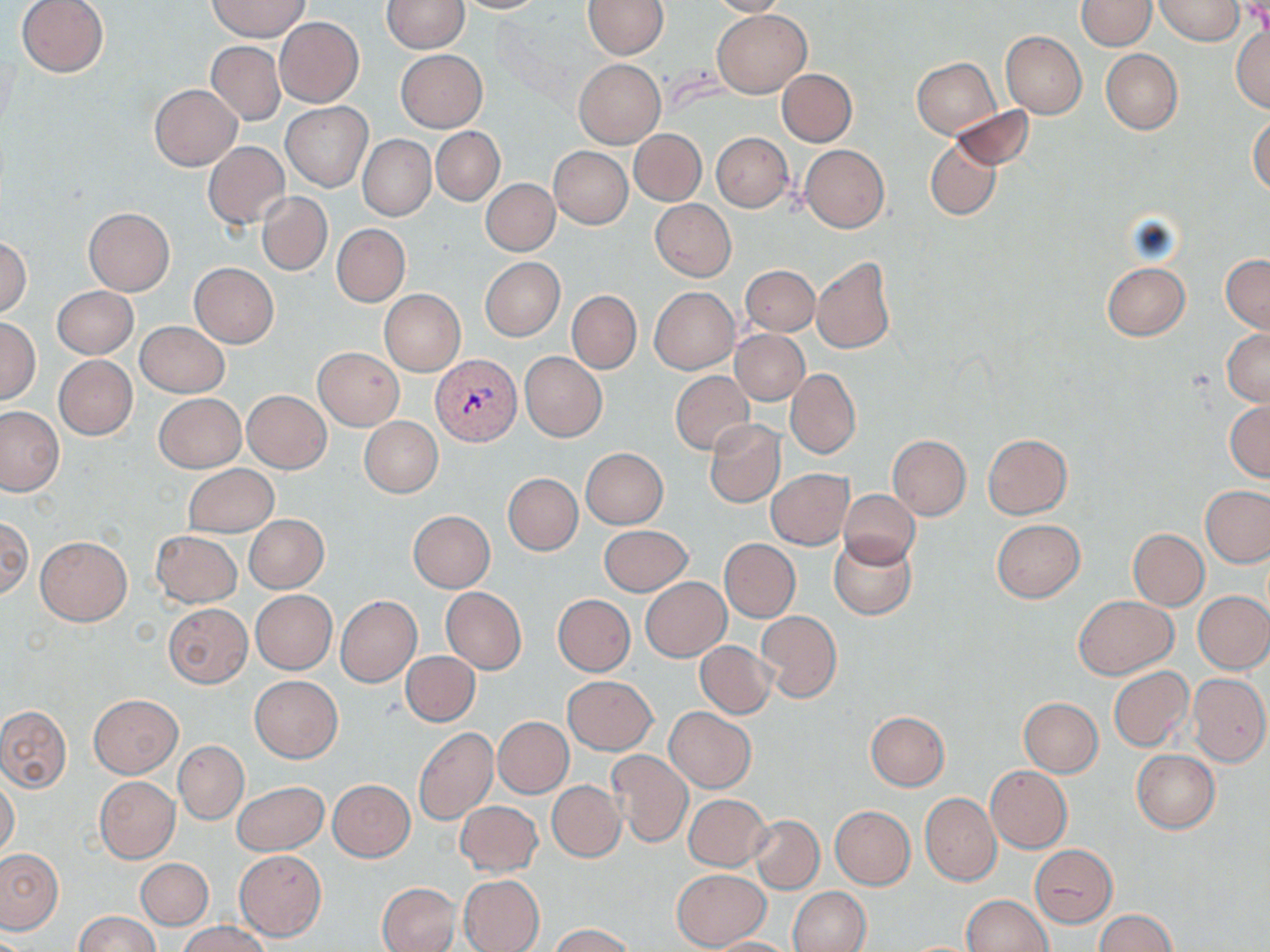

slide_level_diagnosis: Plasmodium vivax
magnification: 1000x
field_of_view: one of a larger specimen
preparation: thin blood film
uninfected_red_blood_cell_locations: 'approximate bounding boxes as (x1, y1, x2, y2) in pixels: (16, 0, 109, 77), (452, 0, 549, 13), (709, 0, 791, 17), (1076, 0, 1156, 50), (1156, 0, 1244, 46), (210, 1, 308, 40), (381, 1, 469, 52), (581, 1, 667, 58), (712, 9, 811, 98), (275, 16, 365, 106), (1231, 24, 1270, 113), (1001, 30, 1087, 118), (206, 41, 285, 125), (395, 49, 488, 132), (1101, 49, 1182, 134), (911, 57, 1000, 139), (573, 58, 666, 149), (777, 69, 856, 146), (149, 84, 241, 170), (281, 102, 371, 190), (948, 106, 1034, 172), (1249, 114, 1270, 195), (431, 126, 505, 206), (629, 129, 707, 206), (711, 133, 793, 212), (358, 135, 435, 221), (925, 136, 1002, 220), (203, 142, 290, 230), (801, 145, 890, 232), (550, 147, 633, 228), (482, 179, 559, 256), (257, 191, 332, 276), (650, 199, 736, 281), (84, 207, 175, 294), (331, 224, 410, 307), (0, 235, 32, 318), (1221, 253, 1270, 334), (812, 256, 896, 354), (480, 257, 565, 341), (1101, 261, 1190, 340), (189, 263, 279, 347), (742, 265, 819, 336), (52, 286, 138, 359), (650, 287, 739, 374), (379, 289, 466, 376), (567, 291, 641, 373), (0, 318, 40, 403), (135, 321, 229, 397), (730, 329, 809, 405), (1222, 329, 1270, 405), (313, 347, 404, 429), (520, 352, 606, 441), (54, 355, 137, 440), (786, 370, 860, 456), (670, 372, 754, 454), (242, 391, 331, 473), (154, 393, 246, 472), (1225, 401, 1269, 482), (0, 406, 66, 496), (360, 416, 443, 498), (704, 419, 786, 508), (982, 434, 1072, 518), (886, 435, 971, 520), (581, 448, 667, 528), (182, 464, 278, 537), (766, 469, 853, 548), (503, 472, 582, 555), (1201, 485, 1270, 568), (839, 489, 918, 567), (408, 510, 495, 592), (0, 515, 32, 602), (244, 515, 328, 592), (991, 518, 1084, 603), (599, 525, 692, 596), (1128, 529, 1209, 609), (151, 531, 241, 607), (829, 535, 916, 619), (36, 536, 131, 626), (718, 539, 800, 623), (641, 577, 730, 660), (441, 587, 526, 674), (250, 590, 336, 673), (1193, 592, 1270, 673), (335, 595, 421, 687), (553, 595, 635, 675), (1075, 595, 1177, 678), (164, 603, 252, 688), (757, 610, 842, 703), (696, 641, 776, 718), (402, 651, 479, 726), (1108, 666, 1193, 751), (1189, 673, 1269, 766), (250, 675, 342, 762), (562, 676, 657, 755), (89, 694, 182, 777), (1019, 698, 1102, 777), (0, 705, 71, 792), (665, 707, 756, 792), (866, 711, 949, 791), (493, 716, 573, 798), (413, 726, 497, 824), (173, 740, 249, 825), (605, 750, 692, 848), (1132, 750, 1220, 832), (986, 766, 1072, 853), (94, 777, 179, 863), (0, 778, 20, 859), (328, 780, 415, 861), (233, 781, 329, 855), (547, 781, 625, 861), (920, 792, 1002, 886), (684, 793, 771, 871), (455, 801, 542, 876), (830, 806, 915, 888), (750, 815, 824, 893), (1030, 846, 1117, 927), (0, 848, 65, 935), (233, 849, 327, 940), (136, 858, 213, 929), (672, 869, 770, 949), (458, 874, 544, 952), (377, 883, 460, 952), (787, 887, 871, 952), (962, 895, 1052, 952), (1095, 910, 1177, 952), (74, 912, 161, 952), (177, 922, 269, 952), (550, 923, 635, 952), (706, 937, 800, 952)'
image_size: 1270×952 pixels
modality: optical microscopy
stain: May-Grünwald-Giemsa
plasmodium_vivax_infected_red_blood_cell_locations: 'approximate bounding boxes as (x1, y1, x2, y2) in pixels: (430, 355, 521, 445)'